Assess this cell for malaria.
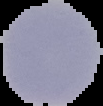
It is uninfected.

Summary:
  - Preparation: thin blood film
  - Image size: 103×106 pixels
  - Image type: cell region segmented out of the field of view; surrounding area masked to black